Classify this cell by malaria status.
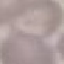

It is uninfected.

Summary:
  - Capture: smartphone camera at the microscope eyepiece
  - Preparation: thin smear
  - Stain: Giemsa
  - Image type: automatically extracted cell patch, resized to 64 × 64 pixels